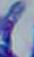

magnification = 1000x
identification = Toxoplasma gondii
modality = photomicrograph